Classify this cell by malaria status.
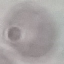
It is uninfected.

Cell patch, automatically extracted from a larger field of view and resized to 64 × 64 pixels. Giemsa-stained preparation. Thin smear of blood. Acquired by smartphone through the microscope eyepiece.